Identify the parasite.
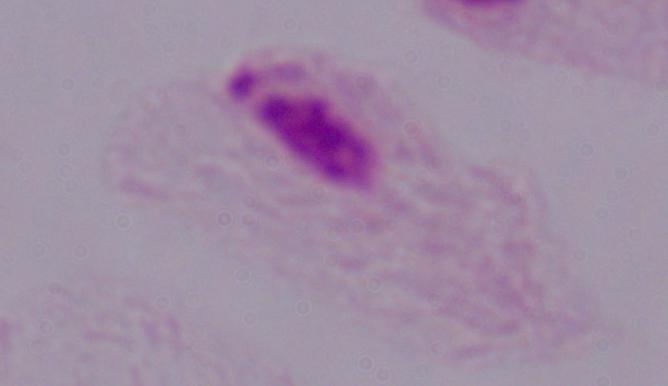

A trichomonad.

magnification: 1000x
modality: photomicrograph